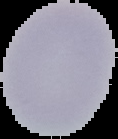

malaria status = uninfected
preparation = thin blood film
image type = segmented cell region with the area outside set to black
image size = 118×139 pixels